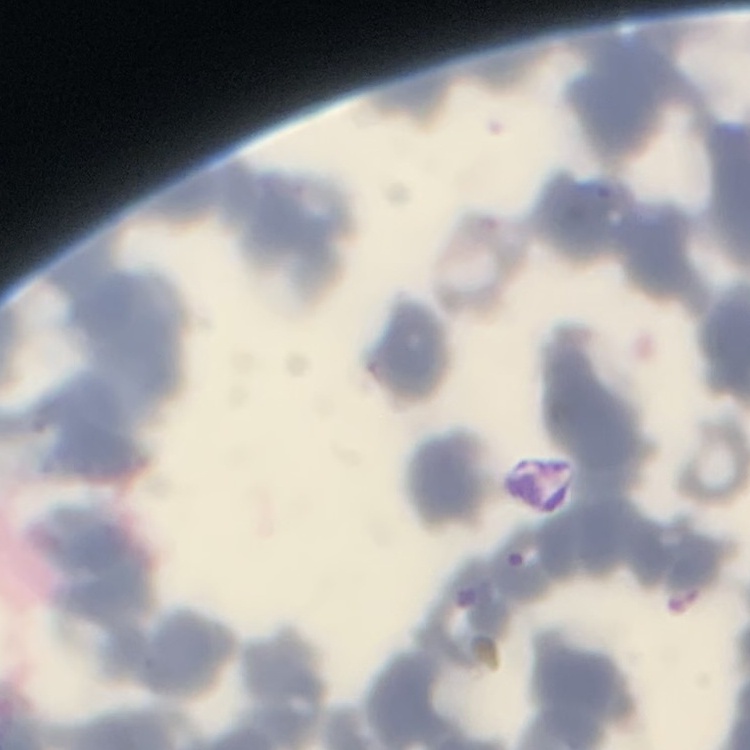
The erythrocytes exhibit rouleaux formation. Field's or Giemsa stain. Square crop of a larger photomicrograph. Thin blood smear.